Describe the morphology of the erythrocytes.
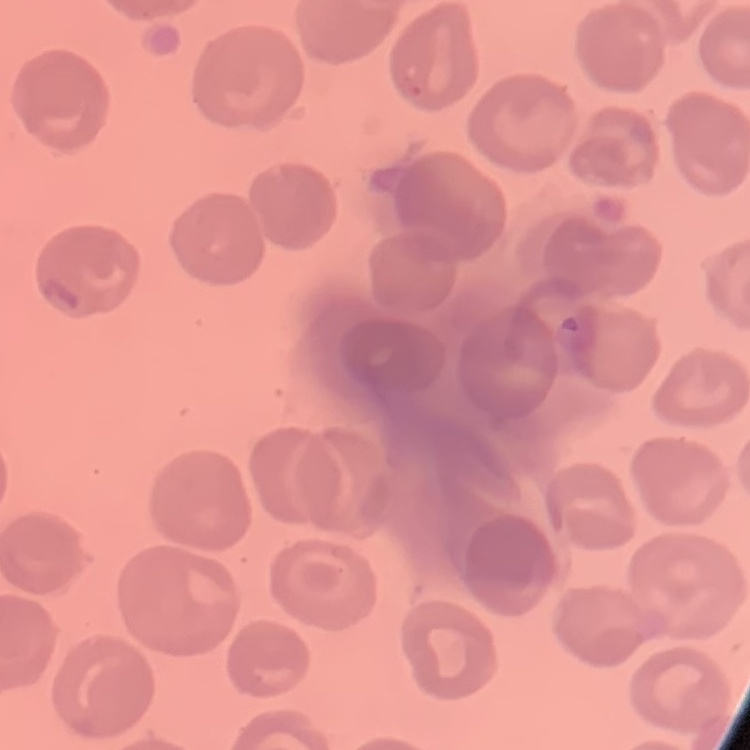

They show no rouleaux formation.

Field's or Giemsa stain. Thin blood film. Square crop of a larger photomicrograph.